Assess this cell for malaria.
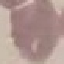

Uninfected.

Cell patch, automatically extracted from a larger field of view and resized to 64 × 64 pixels. Photographed with a smartphone camera at the microscope eyepiece. Giemsa-stained preparation. Thin smear of blood.